Give the extent of all Plasmodium vivax-infected red blood cells.
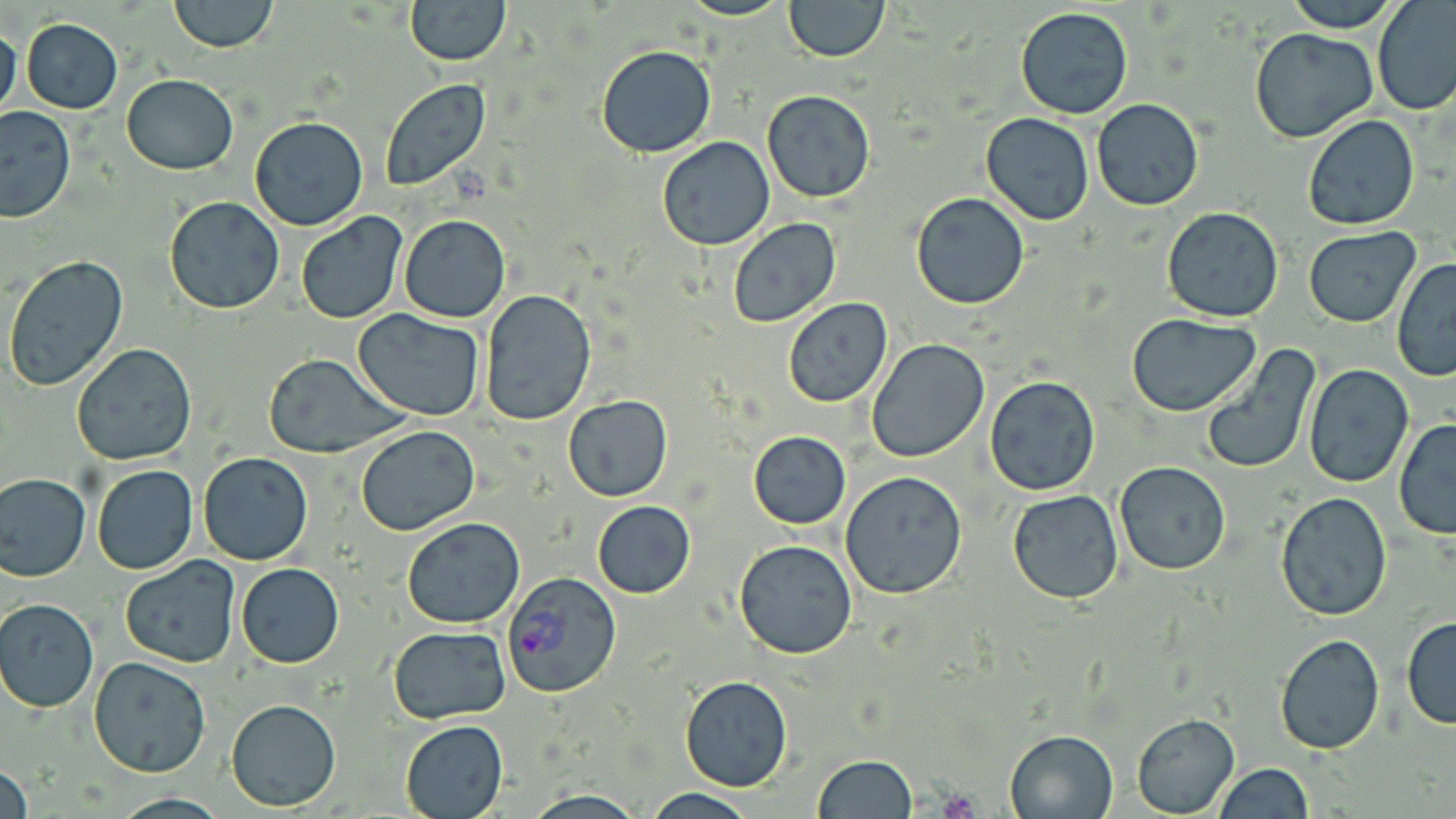

Approximate bounding boxes as (x1, y1, x2, y2) in pixels.
Plasmodium vivax-infected red blood cells: (502, 573, 621, 698).

slide-level diagnosis = Plasmodium vivax
platelet locations = approximate bounding boxes as (x1, y1, x2, y2) in pixels: (936, 789, 984, 819)
preparation = thin blood smear
magnification = 1000x
field of view = single
modality = light microscopy
stain = May-Grünwald-Giemsa
uninfected red blood cell locations = approximate bounding boxes as (x1, y1, x2, y2) in pixels: (167, 0, 277, 53), (406, 0, 509, 66), (678, 0, 794, 21), (783, 0, 888, 61), (1280, 0, 1404, 32), (1372, 0, 1456, 117), (1015, 6, 1134, 120), (22, 19, 122, 112), (0, 23, 22, 123), (1249, 29, 1379, 143), (595, 44, 716, 158), (120, 72, 239, 174), (379, 79, 491, 192), (760, 90, 878, 203), (1090, 98, 1204, 210), (1, 106, 75, 223), (980, 112, 1095, 224), (1300, 115, 1420, 231), (250, 116, 368, 231), (657, 136, 776, 251), (911, 193, 1030, 309), (165, 196, 285, 314), (1161, 207, 1285, 322), (294, 212, 410, 326), (399, 213, 512, 322), (728, 217, 844, 330), (1302, 227, 1420, 327), (2, 255, 129, 393), (1391, 258, 1456, 381), (480, 289, 597, 427), (783, 298, 893, 407), (354, 308, 486, 420), (1126, 315, 1262, 417), (866, 339, 990, 463), (71, 344, 197, 466), (1201, 345, 1321, 475), (265, 354, 404, 458), (1303, 364, 1412, 486), (985, 375, 1101, 496), (563, 395, 673, 502), (1393, 419, 1456, 540), (354, 425, 480, 536), (748, 430, 851, 528), (198, 452, 313, 566), (1115, 462, 1231, 577), (92, 464, 197, 576), (840, 469, 968, 598), (0, 472, 91, 581), (1004, 476, 1232, 588), (1007, 488, 1124, 604), (1276, 492, 1393, 620), (591, 500, 696, 599), (402, 517, 525, 627), (732, 538, 859, 660), (119, 555, 240, 669), (235, 563, 344, 667), (1, 599, 99, 712), (1401, 615, 1456, 730), (388, 626, 511, 723), (1274, 634, 1386, 754), (88, 656, 211, 777), (678, 674, 794, 791), (226, 698, 341, 810), (1131, 714, 1240, 817), (399, 719, 508, 819), (1005, 728, 1119, 818), (812, 756, 918, 818), (1, 763, 32, 819), (1212, 763, 1314, 818), (643, 789, 761, 819), (522, 790, 648, 819)
image size = 1456×819 pixels